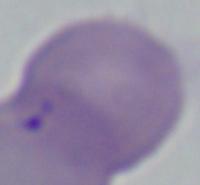

Summary:
  - Modality: micrograph
  - Identification: Babesia
  - Magnification: 1000x